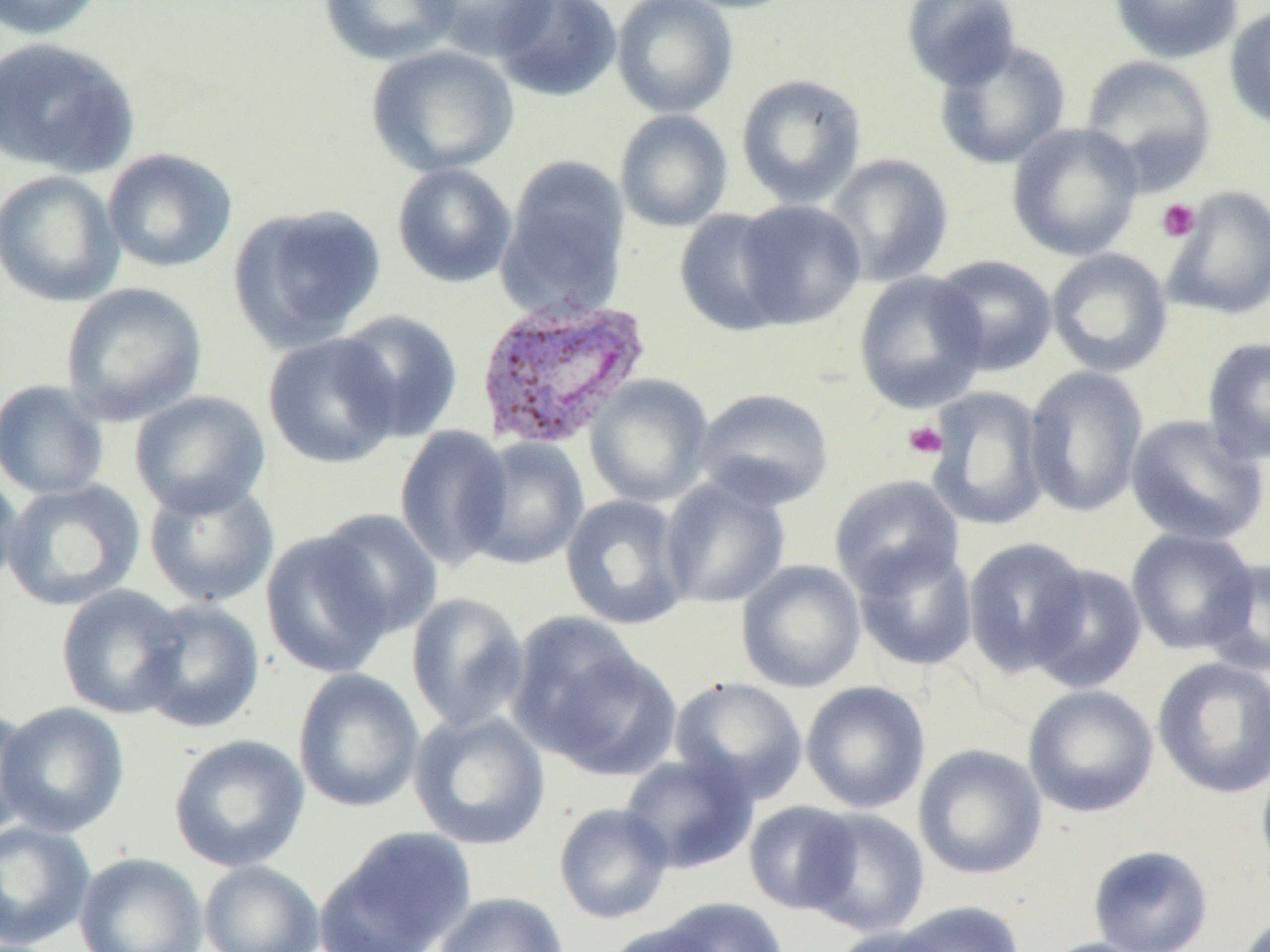

Summary:
  - Coordinate format: approximate bounding boxes as (x1, y1, x2, y2) in pixels
  - Uninfected red blood cell locations: (0, 0, 106, 40), (319, 0, 460, 65), (418, 0, 556, 61), (493, 0, 622, 102), (612, 0, 738, 118), (669, 0, 804, 14), (901, 0, 1022, 91), (1109, 0, 1242, 64), (1224, 6, 1270, 131), (1, 37, 141, 178), (934, 40, 1071, 170), (366, 44, 519, 177), (1079, 54, 1218, 191), (736, 73, 867, 208), (615, 110, 733, 232), (1006, 123, 1145, 261), (101, 148, 237, 274), (825, 153, 954, 286), (497, 159, 631, 319), (391, 163, 518, 288), (0, 170, 125, 307), (1163, 186, 1270, 320), (732, 200, 866, 330), (229, 203, 387, 351), (674, 209, 797, 336), (1046, 248, 1173, 377), (931, 254, 1058, 376), (854, 271, 989, 413), (60, 282, 207, 427), (333, 309, 463, 442), (263, 332, 403, 469), (1202, 337, 1270, 465), (1024, 366, 1149, 517), (585, 374, 713, 507), (0, 380, 110, 500), (926, 386, 1051, 531), (692, 387, 835, 510), (130, 390, 271, 518), (1125, 414, 1267, 547), (394, 425, 513, 571), (464, 437, 590, 570), (0, 469, 23, 592), (829, 475, 965, 597), (659, 477, 791, 609), (1, 479, 145, 612), (144, 479, 279, 608), (560, 494, 690, 630), (312, 508, 443, 639), (1126, 527, 1260, 655), (261, 531, 396, 679), (963, 537, 1092, 676), (853, 544, 979, 671), (1202, 559, 1270, 676), (736, 560, 867, 693), (1026, 563, 1148, 693), (56, 584, 189, 720), (406, 592, 529, 733), (136, 599, 264, 733), (507, 613, 669, 774), (1152, 656, 1270, 799), (293, 669, 424, 813), (669, 676, 808, 805), (801, 680, 931, 814), (1023, 684, 1159, 818), (0, 701, 130, 838), (0, 705, 39, 841), (409, 711, 550, 850), (169, 734, 310, 872), (913, 743, 1048, 880), (1256, 750, 1270, 883), (619, 752, 758, 874), (743, 801, 861, 914), (554, 803, 674, 924), (803, 808, 931, 936), (0, 820, 95, 949), (319, 826, 476, 952), (1087, 845, 1214, 952), (73, 852, 207, 952), (199, 860, 324, 952), (433, 892, 569, 952), (655, 897, 789, 951), (890, 902, 1026, 952), (1231, 914, 1269, 952), (601, 920, 728, 952), (827, 925, 955, 952), (1037, 937, 1159, 952)
  - Plasmodium vivax-infected red blood cell locations: (473, 297, 651, 450)
  - Platelet locations: (1156, 199, 1200, 242), (902, 420, 948, 459)
  - Slide-level diagnosis: Plasmodium vivax
  - Image size: 1270×952 pixels
  - Modality: optical microscopy
  - Field of view: single
  - Preparation: thin blood film
  - Magnification: 1000x